Name the parasite shown.
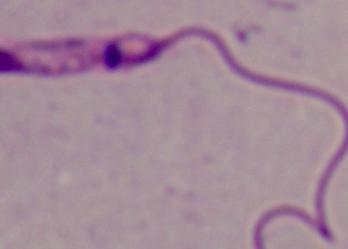
Leishmania.

magnification = 1000x
modality = micrograph